Classify this cell by malaria status.
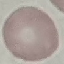
It is uninfected.

Thin blood film. Automatically extracted cell patch, resized to 64 × 64 pixels. Giemsa-stained preparation. Acquired by smartphone through the microscope eyepiece.